Give the extent of all uninfected red blood cells.
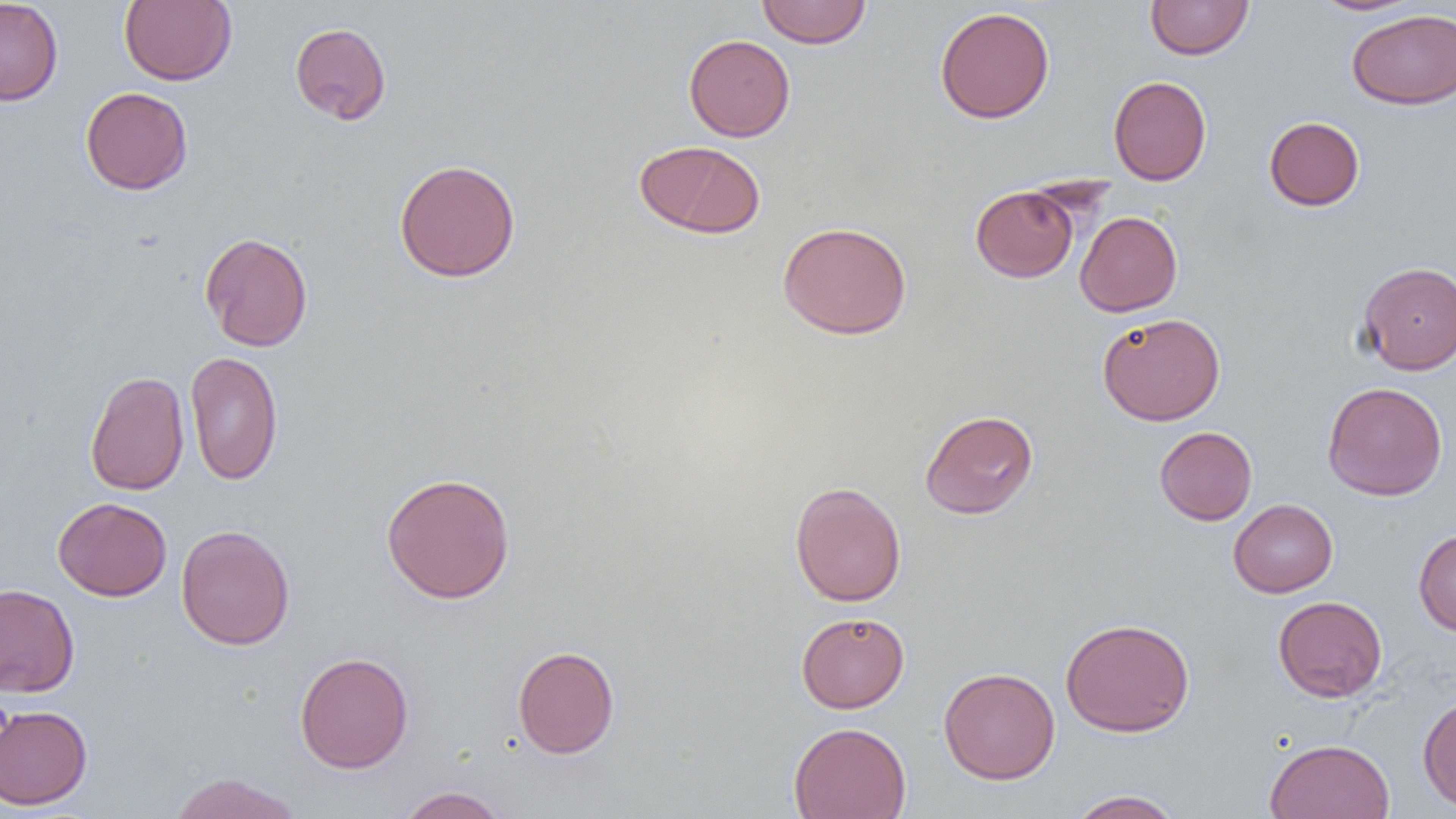

Approximate bounding boxes as (x1,y1)-(x2,y2) corner pairs in pixels.
Uninfected red blood cells: (0,0)-(64,105), (120,0)-(237,86), (757,0)-(871,48), (1145,0)-(1253,60), (1309,0)-(1424,16), (934,6)-(1055,124), (1347,9)-(1456,109), (290,22)-(391,125), (683,34)-(795,141), (1108,75)-(1211,185), (81,87)-(193,195), (1264,116)-(1365,211), (635,139)-(765,239), (393,158)-(521,283), (970,184)-(1079,282), (1075,211)-(1182,316), (778,222)-(912,339), (199,232)-(313,351), (1357,261)-(1455,374), (1097,313)-(1226,426), (185,351)-(283,485), (85,370)-(189,495), (1322,381)-(1448,501), (919,409)-(1039,519), (1154,426)-(1257,525), (380,472)-(516,603), (789,481)-(907,606), (53,497)-(172,601), (1228,498)-(1338,597), (176,524)-(295,650), (1413,529)-(1456,636), (0,582)-(80,697), (1272,595)-(1387,702), (795,611)-(910,713), (1060,617)-(1195,737), (512,645)-(620,758), (294,651)-(414,773), (938,666)-(1060,784), (1417,694)-(1456,813), (0,704)-(93,810), (788,722)-(911,819), (1264,738)-(1395,819), (166,772)-(304,819), (396,786)-(509,819), (1067,789)-(1185,818).

Summary:
  - Slide-level diagnosis: negative for blood parasites
  - Magnification: 1000x
  - Image size: 1456×819 pixels
  - Preparation: thin blood film
  - Modality: optical microscopy
  - Field of view: one of a larger specimen